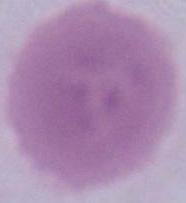
Summary:
  - Magnification: 1000x
  - Identification: red blood cell
  - Modality: micrograph